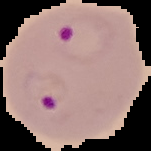

From a thin blood film. Image is 151×151 pixels. Cell region segmented out of the field of view; the surrounding area is masked to black. Result: Plasmodium parasites detected.